Outline each uninfected red blood cell.
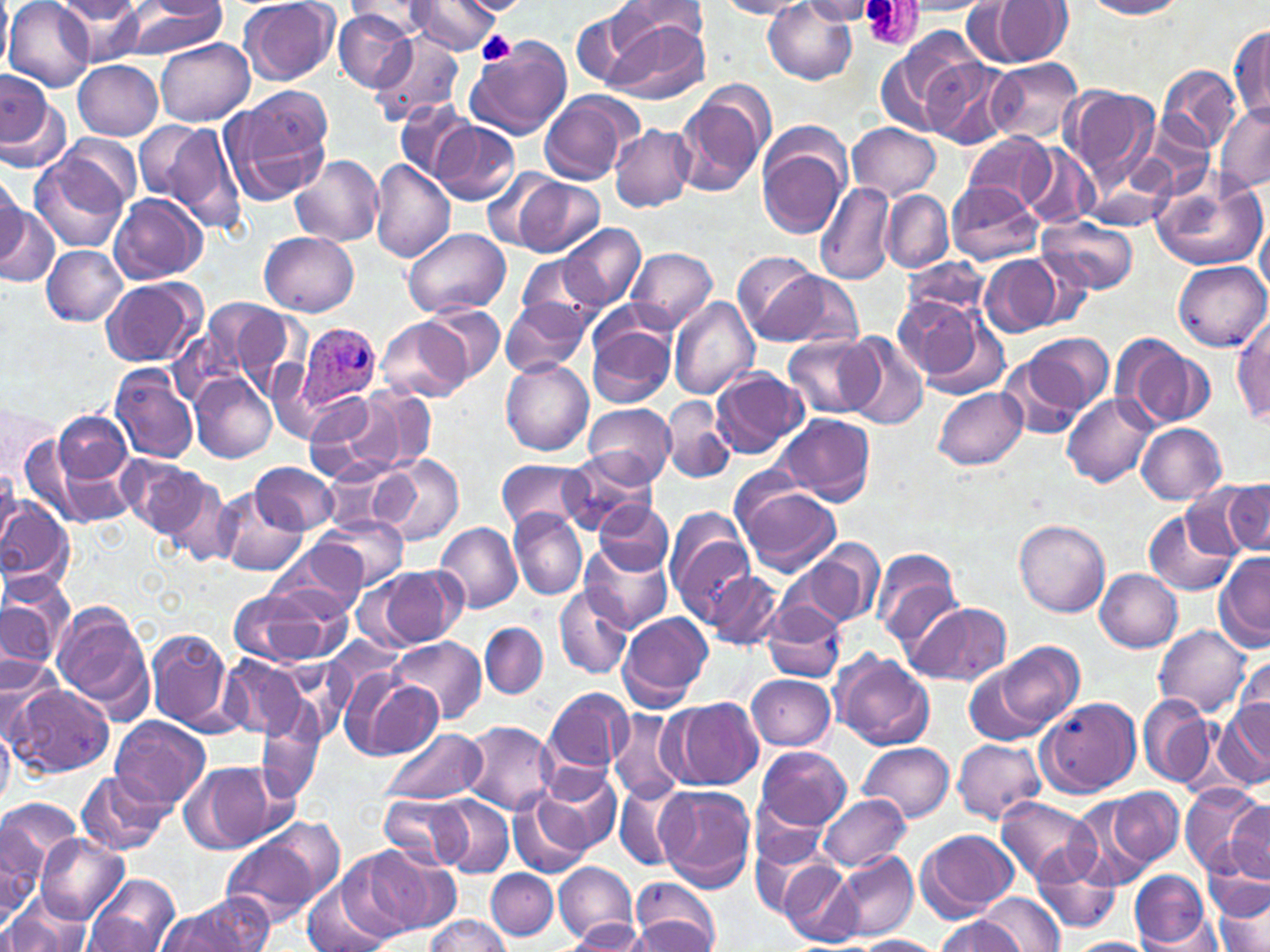
Approximate bounding boxes as [x1, y1, x2, y2] in pixels.
Uninfected red blood cells: [0, 0, 12, 76], [54, 0, 144, 25], [451, 0, 531, 16], [1085, 0, 1189, 18], [5, 1, 94, 90], [56, 1, 151, 64], [239, 1, 340, 86], [616, 1, 711, 45], [716, 1, 813, 19], [764, 1, 858, 84], [798, 1, 879, 24], [896, 1, 995, 16], [974, 1, 1074, 67], [345, 2, 440, 37], [406, 2, 500, 55], [570, 3, 675, 94], [114, 4, 229, 60], [333, 12, 415, 91], [604, 18, 710, 105], [1231, 23, 1270, 119], [368, 32, 468, 126], [877, 32, 983, 134], [463, 38, 572, 144], [156, 39, 254, 126], [920, 58, 1013, 148], [985, 58, 1084, 145], [73, 60, 163, 140], [1157, 63, 1242, 152], [2, 72, 65, 168], [1062, 85, 1160, 183], [673, 87, 771, 196], [222, 90, 332, 205], [539, 91, 641, 186], [396, 100, 475, 183], [1213, 103, 1270, 195], [138, 117, 248, 237], [433, 120, 520, 206], [846, 122, 941, 201], [609, 125, 695, 211], [57, 133, 143, 210], [964, 133, 1056, 210], [757, 136, 848, 240], [1021, 144, 1097, 228], [29, 149, 133, 253], [291, 154, 383, 246], [369, 158, 455, 263], [0, 170, 26, 261], [1150, 172, 1268, 273], [510, 175, 605, 258], [815, 181, 896, 286], [945, 181, 1042, 265], [882, 190, 951, 273], [109, 193, 206, 282], [0, 203, 56, 290], [1257, 215, 1270, 301], [1037, 218, 1138, 297], [561, 221, 645, 310], [401, 228, 510, 318], [261, 232, 359, 317], [41, 245, 128, 326], [626, 246, 719, 332], [520, 252, 600, 323], [738, 252, 828, 342], [907, 255, 988, 321], [980, 255, 1064, 336], [1172, 260, 1268, 352], [768, 269, 863, 347], [101, 277, 205, 367], [890, 294, 989, 384], [668, 296, 759, 399], [501, 298, 590, 377], [199, 299, 295, 394], [427, 304, 505, 381], [1233, 314, 1270, 424], [377, 318, 472, 402], [587, 322, 675, 408], [1017, 331, 1114, 422], [786, 334, 879, 419], [1110, 334, 1213, 430], [844, 335, 928, 429], [997, 352, 1094, 441], [266, 359, 328, 445], [500, 359, 594, 455], [108, 365, 197, 463], [711, 368, 809, 459], [190, 376, 277, 462], [349, 387, 436, 475], [932, 387, 1027, 469], [300, 390, 372, 448], [1061, 393, 1157, 488], [319, 395, 403, 481], [661, 397, 735, 484], [0, 401, 58, 477], [583, 402, 675, 486], [53, 409, 133, 486], [776, 413, 877, 505], [13, 423, 81, 516], [1137, 424, 1227, 504], [27, 441, 132, 526], [564, 452, 654, 534], [119, 454, 207, 537], [379, 454, 464, 546], [323, 455, 410, 536], [498, 458, 591, 534], [251, 462, 339, 535], [0, 469, 20, 549], [159, 472, 240, 567], [1218, 478, 1270, 558], [734, 483, 841, 576], [216, 490, 306, 577], [0, 497, 75, 597], [594, 500, 672, 574], [1142, 507, 1239, 597], [508, 509, 587, 600], [315, 514, 409, 590], [665, 514, 755, 618], [1014, 519, 1109, 616], [436, 521, 524, 613], [582, 538, 673, 635], [794, 539, 884, 628], [270, 544, 367, 620], [869, 546, 963, 649], [1214, 552, 1270, 652], [377, 567, 465, 646], [1096, 568, 1183, 652], [3, 571, 75, 657], [706, 572, 785, 649], [233, 583, 350, 669], [554, 585, 632, 678], [761, 600, 845, 683], [904, 600, 1013, 687], [0, 601, 55, 682], [52, 601, 154, 720], [618, 612, 712, 711], [479, 621, 548, 699], [1153, 624, 1252, 716], [146, 627, 235, 734], [389, 637, 485, 725], [321, 638, 407, 713], [989, 639, 1084, 735], [832, 651, 936, 750], [0, 653, 62, 744], [1233, 654, 1269, 740], [218, 655, 309, 742], [966, 664, 1053, 746], [338, 665, 413, 754], [748, 673, 836, 750], [360, 678, 443, 757], [8, 684, 114, 777], [546, 688, 633, 774], [1137, 694, 1216, 789], [663, 696, 763, 790], [1036, 697, 1141, 797], [1213, 700, 1270, 793], [255, 709, 324, 803], [609, 710, 684, 806], [109, 716, 211, 809], [460, 721, 557, 815], [0, 724, 15, 805], [383, 728, 485, 805], [952, 738, 1045, 823], [858, 742, 955, 825], [755, 746, 851, 830], [179, 761, 285, 854], [535, 766, 623, 855], [77, 769, 170, 854], [1182, 783, 1265, 876], [615, 784, 690, 872], [657, 786, 756, 892], [1111, 787, 1183, 866], [379, 794, 471, 871], [508, 794, 590, 880], [818, 794, 911, 872], [430, 795, 514, 877], [997, 796, 1100, 884], [749, 797, 832, 880], [1, 798, 84, 877], [1073, 798, 1160, 889], [1226, 800, 1270, 880], [0, 813, 58, 917], [917, 828, 1018, 920], [219, 829, 331, 928], [36, 833, 128, 923], [1206, 839, 1269, 923], [345, 844, 453, 938], [832, 851, 918, 940], [1035, 854, 1122, 932], [780, 859, 861, 945], [554, 861, 637, 942], [486, 869, 557, 939], [1129, 870, 1213, 948], [84, 874, 181, 952], [303, 876, 399, 952], [627, 879, 722, 952], [978, 892, 1065, 952], [1213, 895, 1269, 952], [1, 896, 92, 952], [155, 900, 264, 952], [84, 914, 161, 949], [424, 915, 510, 951], [634, 915, 718, 950], [932, 915, 1026, 952], [569, 919, 646, 949], [1136, 926, 1228, 950], [849, 935, 946, 952], [1064, 937, 1153, 952].

Summary:
  - Platelet locations: [476, 31, 516, 67]
  - Plasmodium ovale-infected red blood cell locations: [298, 324, 381, 411]
  - Slide-level diagnosis: Plasmodium ovale
  - Stain: May-Grünwald-Giemsa
  - Preparation: thin blood smear
  - Magnification: 1000x
  - Modality: light microscopy
  - Field of view: single
  - Image size: 1270×952 pixels